Locate malaria parasites and leukocytes.
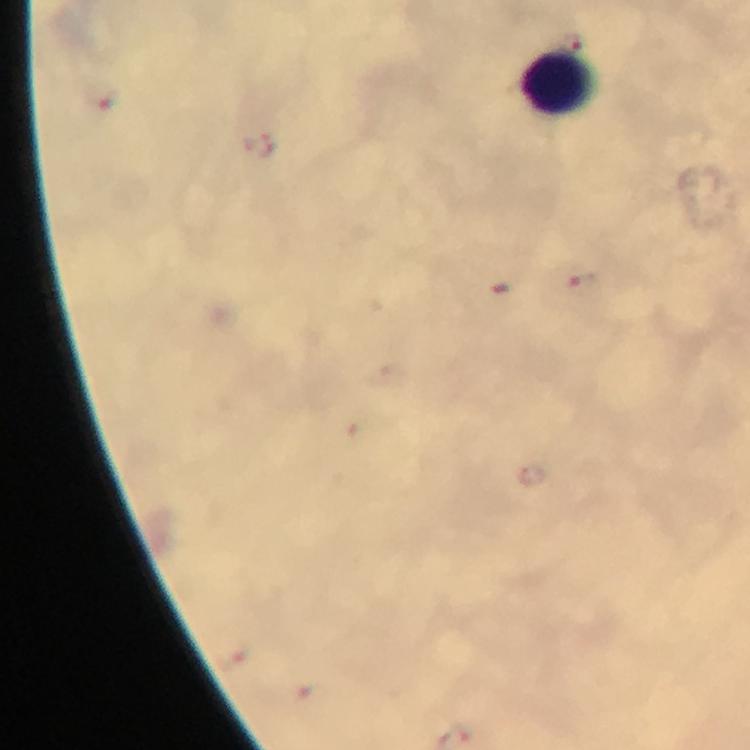
Approximate centers as {x, y} in pixels.
Malaria parasites: {586, 286}.
Leukocytes: {560, 84}.

Photographed with a smartphone mounted on the microscope. 100x magnification. From a malaria diagnostic workup. Immersion oil applied. Image is 750×750 pixels. Cropped region of a single field of view. Giemsa-stained preparation. Thick smear.